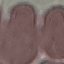
Summary:
  - Result: no malaria parasites detected
  - Image type: automatically extracted cell patch, resized to 64 × 64 pixels
  - Preparation: thin smear
  - Stain: Giemsa
  - Capture: smartphone camera at the microscope eyepiece